Give the position of every Plasmodium parasite.
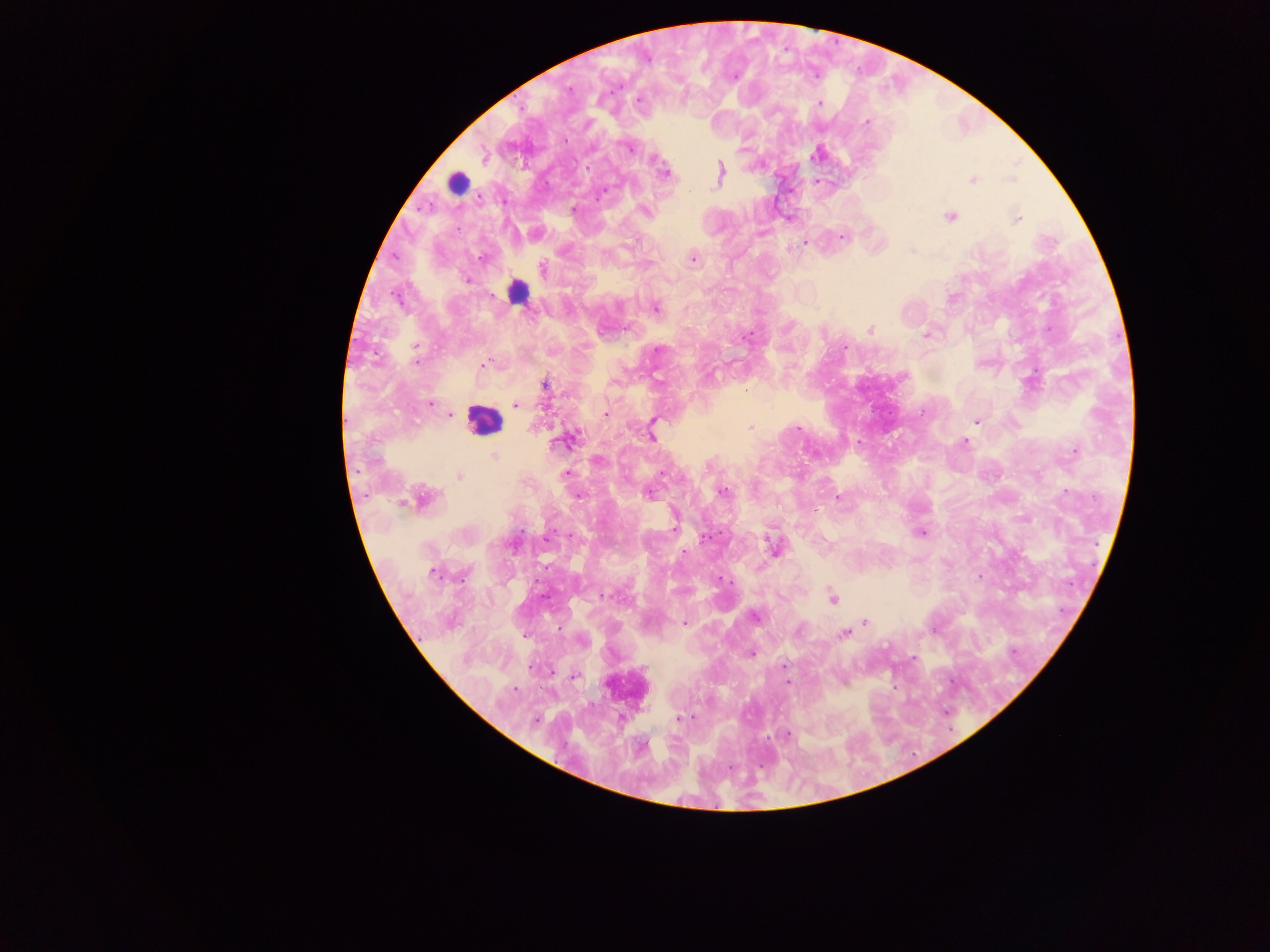
Approximate centers as [x, y] in pixels.
Plasmodium parasites: [734, 78], [569, 88], [638, 101], [819, 104], [866, 121], [565, 139], [628, 147], [484, 158], [587, 168], [720, 171], [665, 173], [1012, 178], [972, 180], [690, 190], [600, 196], [574, 209], [644, 210], [950, 217], [1016, 219], [841, 236], [805, 243], [480, 259], [692, 259], [543, 269], [466, 280], [655, 308], [870, 330], [926, 334], [844, 346], [416, 348], [659, 350], [415, 358], [483, 365], [544, 384], [430, 404], [516, 405], [922, 412], [605, 413], [450, 414], [976, 421], [652, 426], [750, 427], [798, 428], [651, 435], [569, 439], [965, 442], [1075, 451], [495, 456], [599, 461], [566, 474], [663, 474], [459, 476], [722, 491], [648, 494], [577, 495], [838, 498], [424, 499], [674, 526], [921, 533], [570, 536], [705, 537], [547, 539], [772, 545], [685, 552], [433, 573], [605, 595], [833, 599], [754, 616], [865, 621], [684, 624], [799, 631], [844, 633], [751, 654], [784, 666], [575, 676], [787, 682], [513, 690], [680, 718], [535, 720], [787, 735].

{
  "leukocyte_locations": "approximate centers as [x, y] in pixels: [457, 183], [517, 291], [483, 419]",
  "capture": "mobile-phone photograph through a microscope",
  "preparation": "thick blood smear",
  "image_size": "1270×952 pixels",
  "country": "Ghana",
  "field_of_view": "single"
}